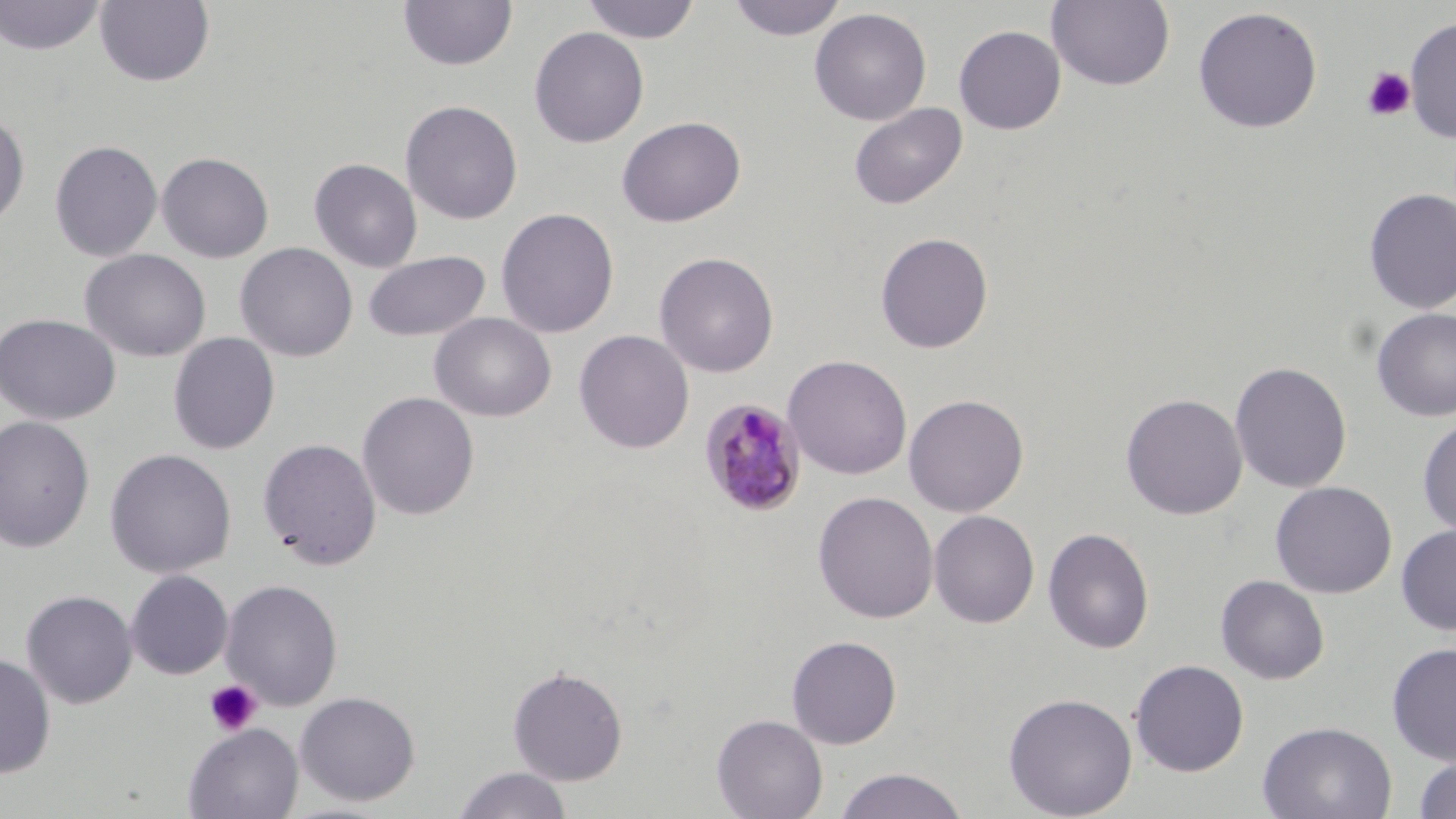 Approximate bounding boxes as [x1, y1, x2, y2] in pixels. Platelet locations: [1362, 67, 1415, 121], [204, 680, 262, 736]. Plasmodium malariae-infected red blood cell locations: [697, 398, 809, 517]. Uninfected red blood cell locations: [0, 0, 107, 56], [398, 0, 518, 71], [581, 0, 701, 44], [727, 0, 847, 41], [1047, 0, 1176, 91], [95, 1, 215, 86], [1192, 6, 1323, 133], [809, 8, 932, 125], [1404, 16, 1456, 143], [953, 25, 1066, 135], [528, 26, 650, 148], [400, 99, 523, 224], [848, 102, 967, 210], [0, 111, 29, 229], [617, 116, 746, 227], [49, 140, 163, 262], [156, 151, 274, 262], [309, 157, 422, 272], [1363, 187, 1456, 314], [496, 207, 619, 338], [875, 232, 994, 354], [235, 243, 358, 362], [80, 249, 211, 362], [362, 250, 490, 342], [654, 252, 779, 378], [1370, 307, 1456, 422], [429, 312, 556, 422], [0, 313, 121, 425], [573, 329, 694, 453], [168, 333, 280, 454], [783, 354, 913, 480], [1229, 360, 1352, 493], [357, 391, 479, 520], [1121, 392, 1248, 520], [903, 393, 1029, 517], [0, 415, 95, 553], [1417, 416, 1456, 538], [257, 438, 382, 570], [104, 448, 236, 579], [1270, 480, 1397, 598], [812, 491, 939, 624], [928, 510, 1040, 628], [1396, 524, 1456, 635], [1042, 527, 1154, 655], [125, 570, 234, 679], [1215, 575, 1329, 685], [221, 579, 343, 711], [21, 590, 138, 709], [786, 635, 902, 748], [1387, 642, 1456, 764], [0, 653, 56, 778], [1129, 659, 1249, 777], [507, 665, 629, 785], [294, 691, 421, 806], [1003, 692, 1138, 819], [711, 714, 828, 819], [1257, 719, 1397, 819], [183, 723, 303, 819], [1412, 754, 1456, 819], [452, 767, 574, 819], [834, 767, 969, 819]. Slide-level diagnosis: Plasmodium malariae. Optical microscopy. Thin blood smear. Single field of view. May-Grünwald-Giemsa stain. Captured at 1000x magnification. Image is 1456×819 pixels.